Assess this cell for malaria.
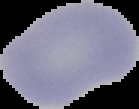
Uninfected.

image_type: segmented cell region with the area outside set to black
image_size: 139×109 pixels
preparation: thin blood smear